Name the parasite shown.
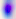

This is Toxoplasma gondii.

modality = micrograph
magnification = 400x